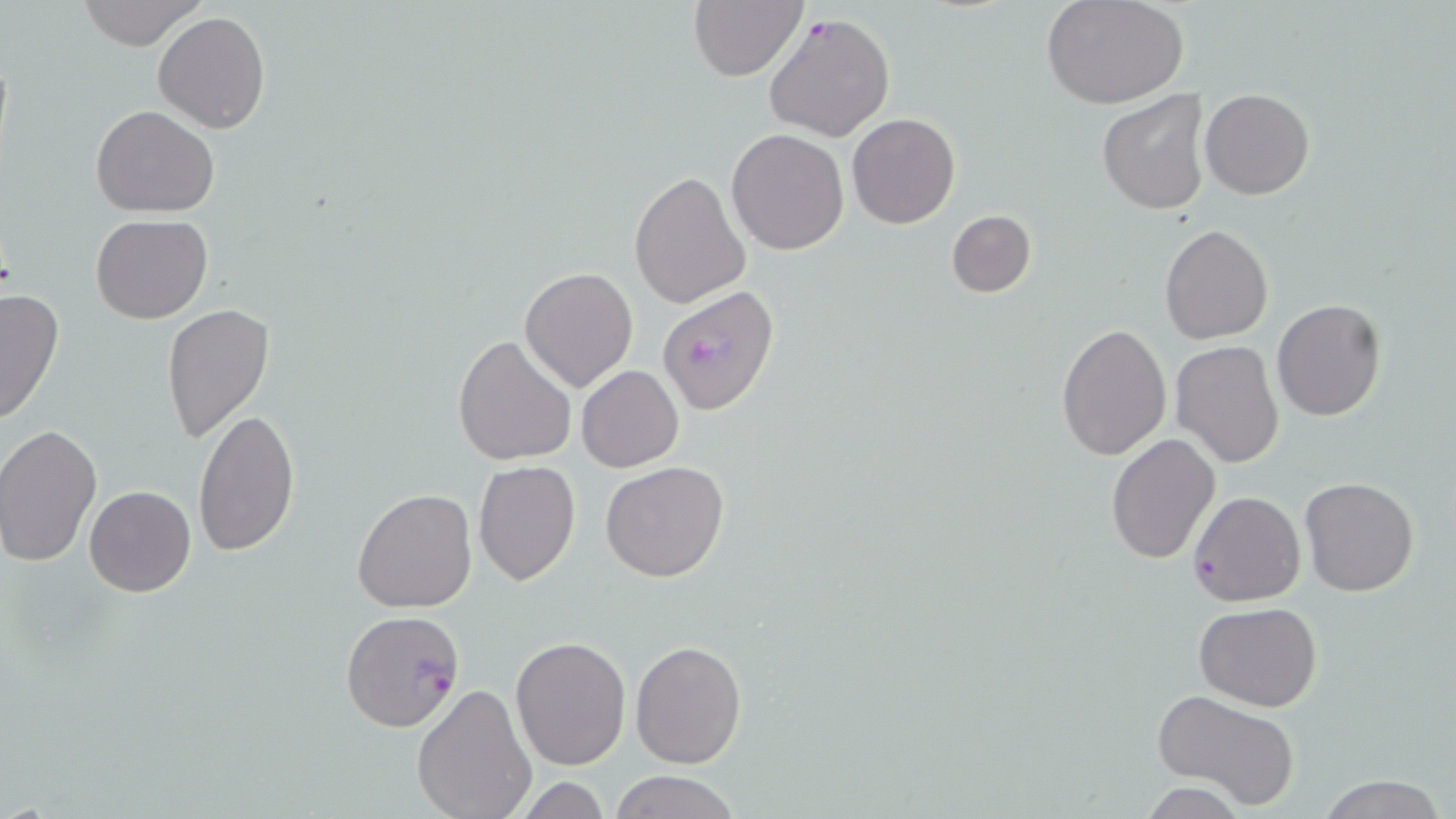

Approximate bounding boxes as (x1, y1, x2, y2) in pixels. Uninfected red blood cell locations: (76, 0, 204, 50), (689, 0, 808, 81), (1044, 1, 1188, 109), (153, 10, 270, 134), (1200, 89, 1315, 200), (1097, 90, 1211, 215), (91, 104, 220, 217), (847, 112, 960, 229), (726, 128, 849, 255), (628, 170, 748, 309), (946, 209, 1036, 298), (91, 213, 214, 324), (1158, 224, 1274, 345), (519, 266, 638, 395), (0, 287, 65, 426), (1272, 299, 1388, 421), (161, 303, 275, 443), (1056, 323, 1171, 461), (454, 334, 578, 467), (1170, 341, 1284, 467), (576, 365, 684, 472), (192, 407, 299, 555), (1, 424, 101, 566), (1105, 433, 1221, 565), (473, 459, 581, 585), (600, 461, 730, 583), (1298, 476, 1420, 597), (85, 485, 196, 596), (351, 488, 476, 612), (1188, 490, 1306, 607), (1194, 603, 1323, 711), (511, 636, 631, 770), (629, 640, 746, 768), (411, 684, 538, 819), (1150, 688, 1301, 810), (608, 769, 741, 819), (1313, 775, 1450, 818), (509, 776, 618, 817), (1136, 782, 1252, 818). Plasmodium falciparum-infected red blood cell locations: (763, 12, 894, 142), (657, 286, 780, 415), (341, 611, 466, 731). Slide-level diagnosis: Plasmodium falciparum. May-Grünwald-Giemsa stain. One field of a larger specimen. Light microscopy. 1000x magnification. Image is 1456×819 pixels. Thin blood film.